Comment on the morphology of the erythrocytes.
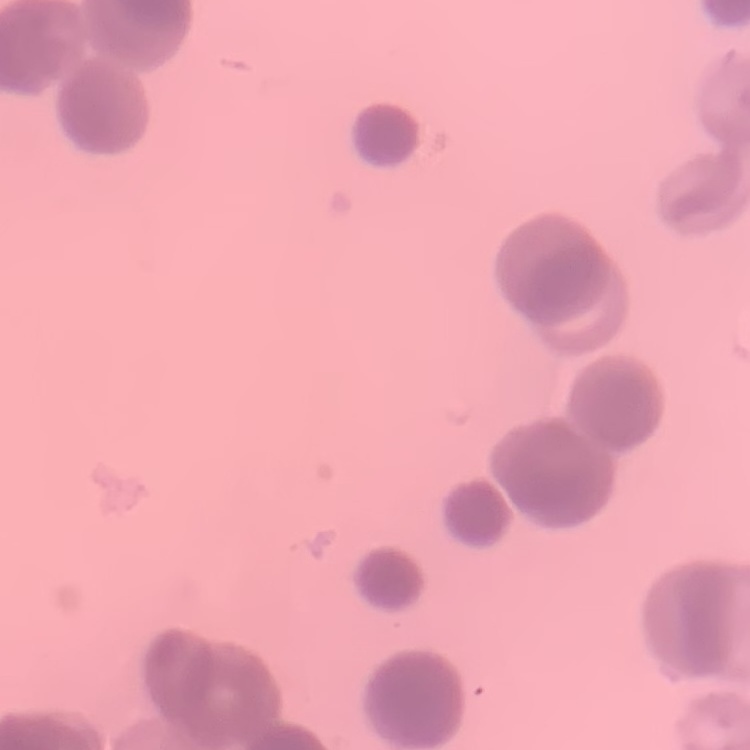

Rouleaux formation.

Thin peripheral smear. Field's or Giemsa stain. Square crop of a larger photomicrograph.